Assess this cell for malaria.
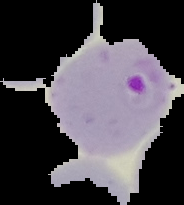
Parasitized.

Summary:
  - Image type: segmented cell region on a black background
  - Preparation: thin blood film
  - Image size: 184×205 pixels